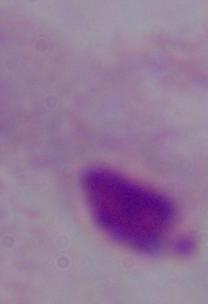
identification: trichomonad
modality: photomicrograph
magnification: 1000x